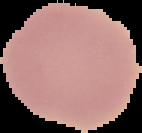

image size = 142×133 pixels
image type = segmented cell region on a black background
malaria status = uninfected
preparation = thin blood film